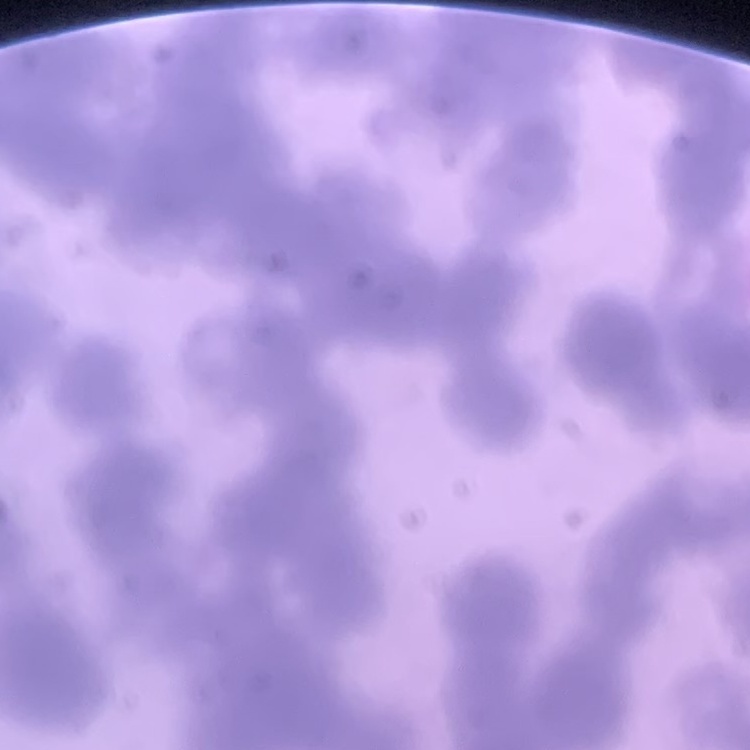
erythrocyte morphology = rouleaux formation
stain = Field's or Giemsa
image type = square crop of a larger photomicrograph
preparation = thin blood smear